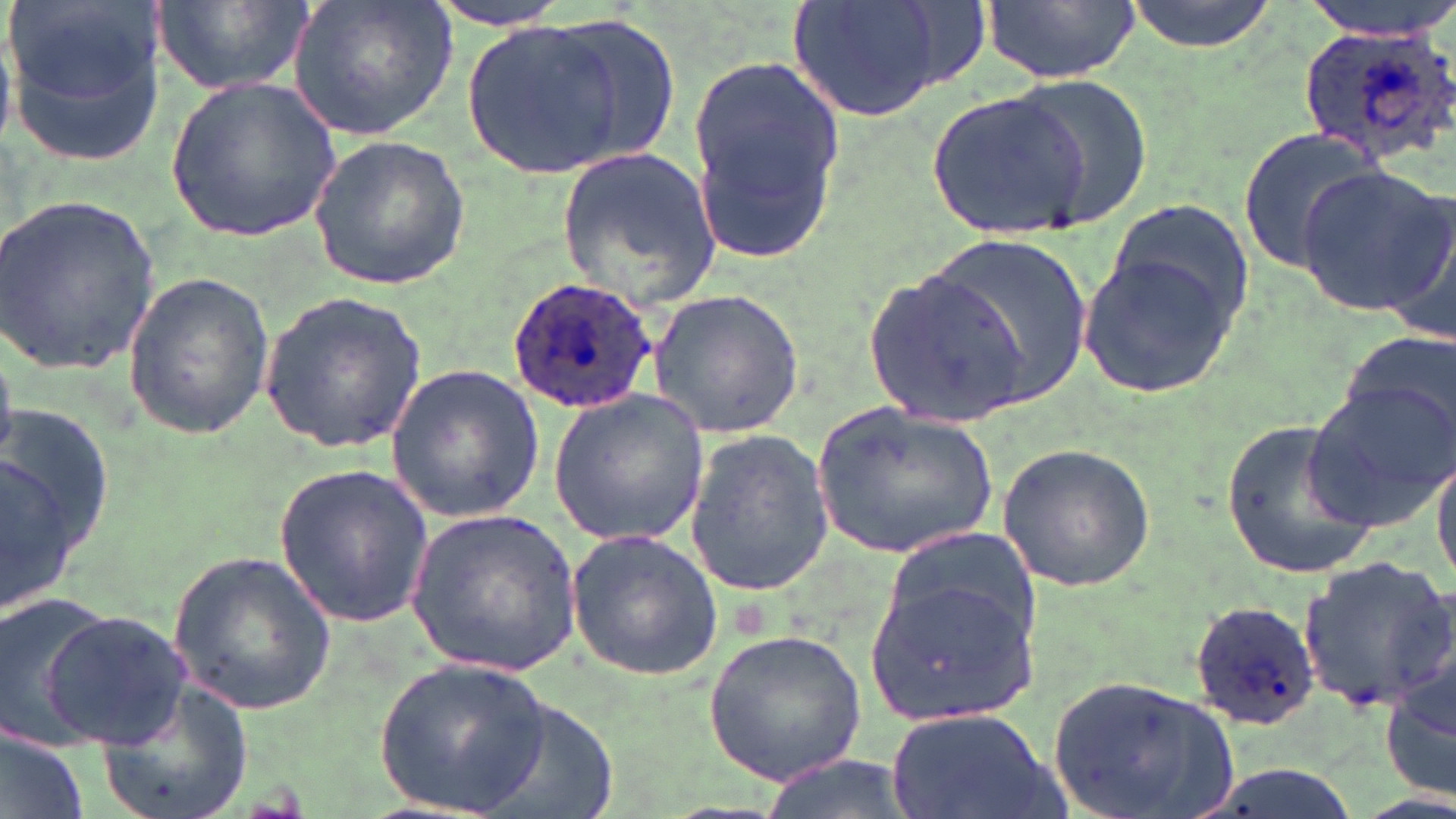

Summary:
  - Coordinate format: approximate bounding boxes as (x1, y1, x2, y2) in pixels
  - Uninfected red blood cell locations: (7, 0, 167, 166), (151, 0, 317, 98), (287, 0, 458, 141), (418, 0, 577, 31), (780, 0, 974, 121), (981, 0, 1136, 84), (1118, 0, 1287, 53), (1300, 0, 1456, 38), (538, 15, 683, 171), (461, 19, 624, 178), (685, 52, 846, 262), (1005, 75, 1152, 225), (163, 76, 341, 243), (928, 88, 1093, 240), (1236, 127, 1381, 278), (308, 136, 469, 291), (553, 146, 721, 311), (1294, 164, 1452, 317), (0, 194, 162, 374), (1105, 199, 1254, 339), (1376, 202, 1456, 345), (922, 236, 1093, 403), (1080, 250, 1240, 399), (863, 265, 1028, 430), (120, 271, 274, 438), (645, 288, 807, 439), (258, 290, 428, 452), (1337, 330, 1456, 445), (386, 362, 545, 524), (1301, 380, 1456, 537), (547, 389, 708, 547), (809, 403, 997, 561), (2, 404, 109, 620), (1222, 417, 1377, 582), (684, 427, 838, 599), (993, 443, 1159, 593), (1431, 446, 1456, 589), (271, 464, 438, 628), (405, 509, 581, 678), (565, 527, 726, 681), (881, 529, 1038, 638), (166, 547, 337, 718), (1297, 555, 1456, 708), (869, 572, 1038, 724), (0, 593, 122, 750), (41, 607, 192, 751), (703, 629, 868, 784), (1383, 647, 1456, 807), (374, 658, 550, 817), (1043, 675, 1237, 819), (93, 682, 252, 819), (888, 708, 1056, 819), (1, 731, 91, 819), (755, 753, 914, 819)
  - Plasmodium ovale-infected red blood cell locations: (1295, 21, 1456, 170), (506, 274, 663, 412), (1190, 599, 1320, 728)
  - Slide-level diagnosis: Plasmodium ovale
  - Image size: 1456×819 pixels
  - Field of view: one of a larger specimen
  - Modality: optical microscopy
  - Stain: May-Grünwald-Giemsa
  - Preparation: thin blood film
  - Magnification: 1000x